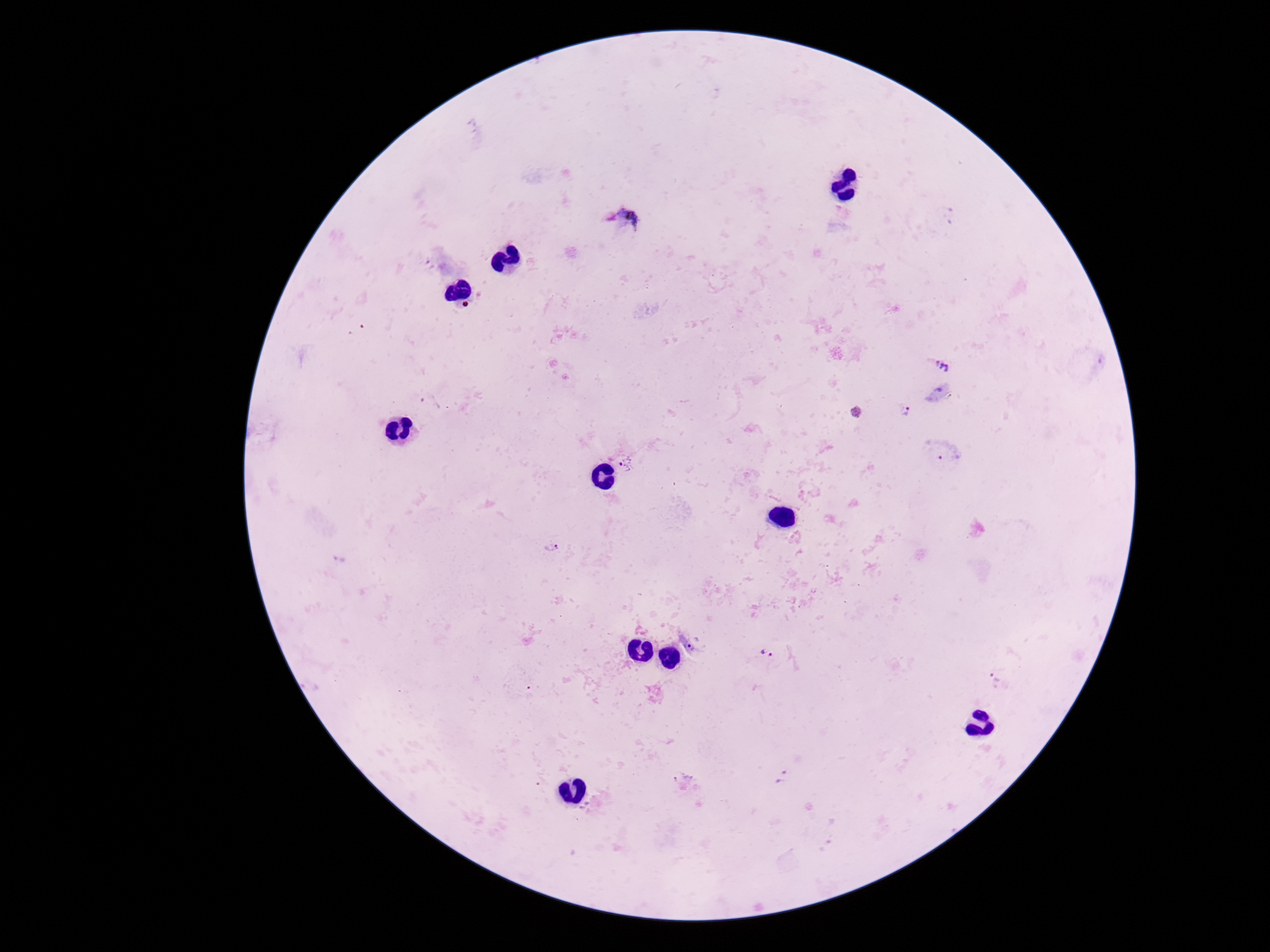

Approximate centers as [x, y] in pixels.
Summary:
  - Plasmodium parasite locations: [950, 215], [624, 222], [944, 364], [430, 403], [905, 412], [856, 414], [949, 456], [629, 465], [552, 547], [340, 560], [695, 643], [767, 653], [997, 679], [781, 777], [681, 779]
  - Field of view: one from this slide
  - Magnification: 100x
  - Image size: 1270×952 pixels
  - Capture: smartphone camera through the microscope eyepiece
  - Stain: Giemsa
  - Preparation: thick blood smear
  - Patient malaria status: infected